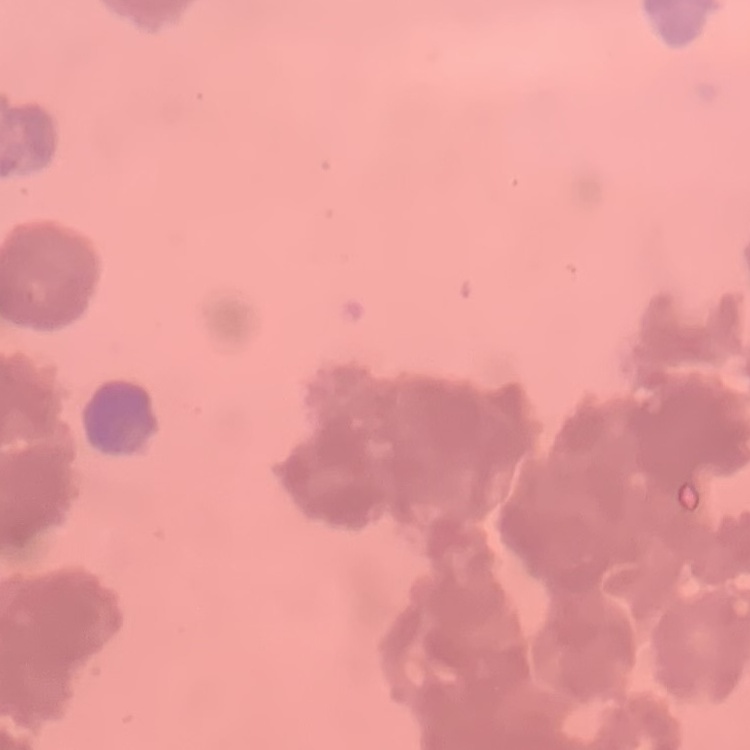

red_blood_cell_morphology: rouleaux formation
image_type: square crop of a larger photomicrograph
preparation: thin blood film
stain: Field's or Giemsa